Identify the cell.
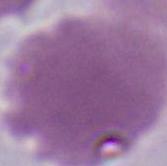

This is an erythrocyte.

Captured at 1000x magnification. Micrograph.